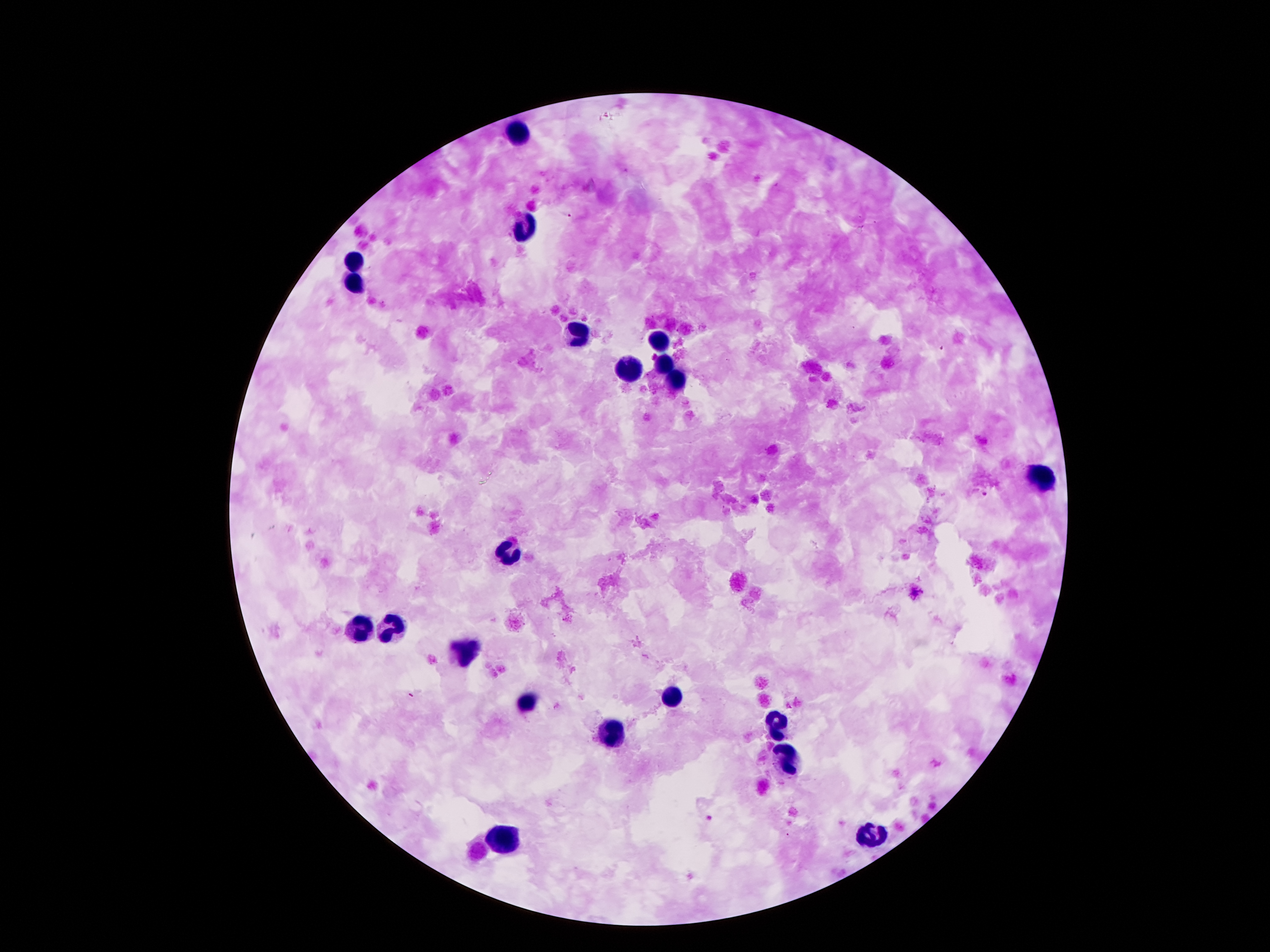

Approximate object centers, in pixels from the top-left corner.
Summary:
  - Leukocyte locations: (x=517, y=131), (x=523, y=228), (x=352, y=261), (x=353, y=282), (x=580, y=335), (x=659, y=341), (x=628, y=367), (x=662, y=367), (x=675, y=380), (x=1039, y=479), (x=509, y=555), (x=358, y=629), (x=391, y=629), (x=465, y=653), (x=673, y=697), (x=530, y=702), (x=777, y=723), (x=609, y=732), (x=788, y=760), (x=502, y=836), (x=872, y=837)
  - Malaria parasite locations: (x=567, y=214), (x=941, y=349), (x=983, y=493), (x=710, y=818)
  - Stain: Giemsa
  - Magnification: 100x
  - Patient malaria status: positive for Plasmodium falciparum
  - Capture: smartphone camera through the microscope eyepiece
  - Image size: 1270×952 pixels
  - Preparation: thick blood smear
  - Field of view: one from this slide